Identify the parasite.
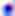
Toxoplasma gondii.

{
  "modality": "photomicrograph",
  "magnification": "400x"
}